Name the parasite shown.
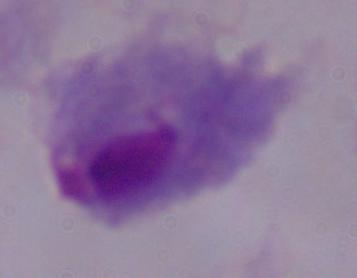

A trichomonad.

modality = micrograph
magnification = 1000x